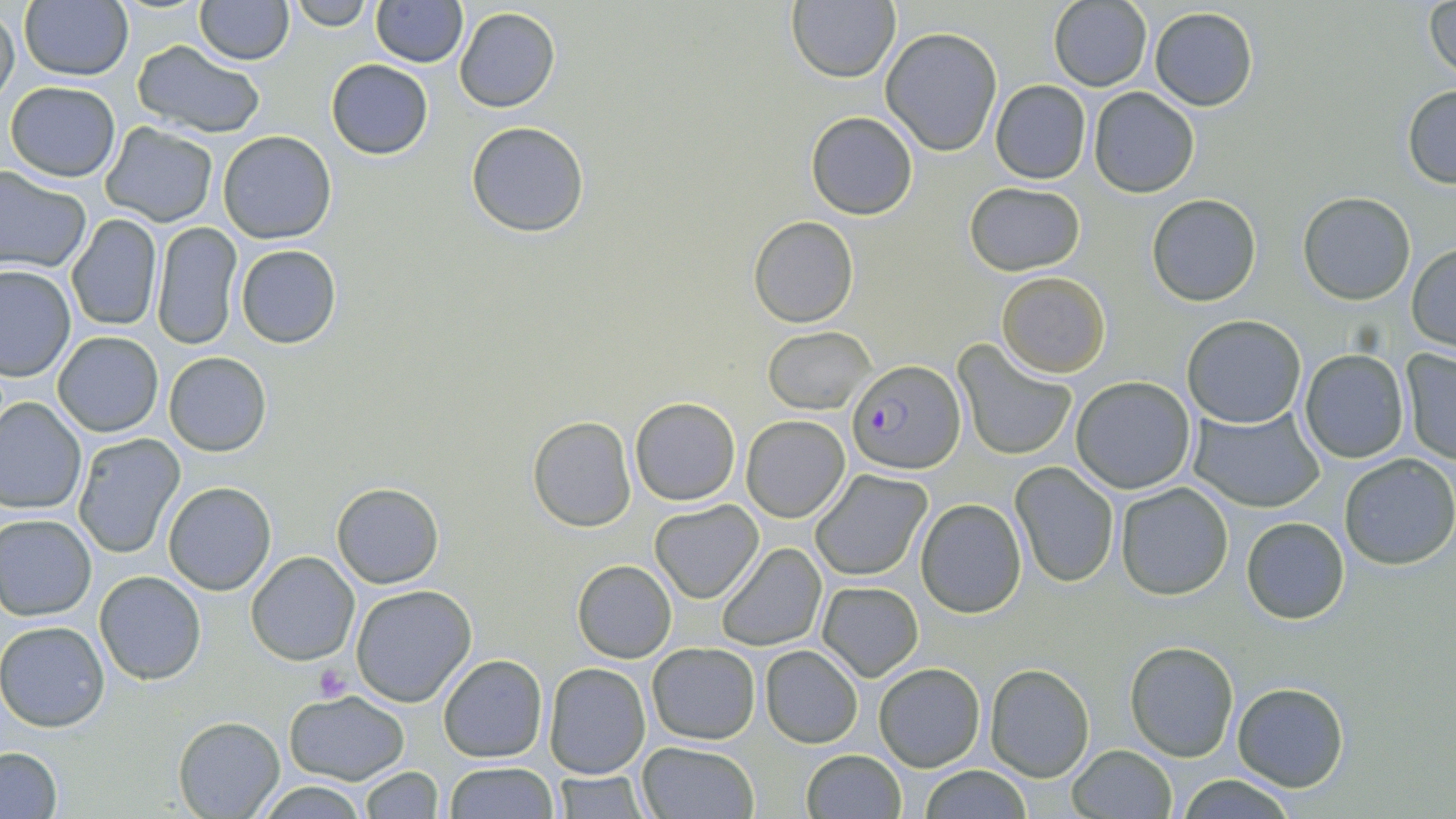
Summary:
  - Coordinate format: approximate bounding boxes as named x1/y1/x2/y2 corners in pixels
  - Platelet locations: (x1=312, y1=664, x2=351, y2=704)
  - Uninfected red blood cell locations: (x1=194, y1=0, x2=294, y2=65), (x1=291, y1=0, x2=375, y2=31), (x1=370, y1=0, x2=466, y2=67), (x1=1426, y1=0, x2=1456, y2=84), (x1=19, y1=1, x2=134, y2=82), (x1=359, y1=1, x2=457, y2=135), (x1=787, y1=1, x2=899, y2=82), (x1=1047, y1=1, x2=1153, y2=91), (x1=0, y1=7, x2=20, y2=109), (x1=454, y1=7, x2=560, y2=113), (x1=1149, y1=8, x2=1258, y2=111), (x1=881, y1=28, x2=1001, y2=157), (x1=133, y1=39, x2=263, y2=137), (x1=326, y1=59, x2=434, y2=159), (x1=5, y1=80, x2=121, y2=181), (x1=991, y1=81, x2=1091, y2=184), (x1=1403, y1=86, x2=1456, y2=188), (x1=1088, y1=88, x2=1198, y2=198), (x1=806, y1=111, x2=918, y2=221), (x1=466, y1=122, x2=591, y2=237), (x1=102, y1=123, x2=217, y2=228), (x1=218, y1=131, x2=337, y2=244), (x1=0, y1=167, x2=92, y2=274), (x1=964, y1=181, x2=1086, y2=275), (x1=1297, y1=192, x2=1417, y2=305), (x1=1147, y1=193, x2=1261, y2=306), (x1=64, y1=215, x2=163, y2=332), (x1=749, y1=216, x2=859, y2=329), (x1=151, y1=222, x2=242, y2=350), (x1=234, y1=244, x2=341, y2=349), (x1=1407, y1=245, x2=1456, y2=350), (x1=0, y1=265, x2=75, y2=381), (x1=994, y1=270, x2=1110, y2=378), (x1=1181, y1=314, x2=1307, y2=428), (x1=764, y1=327, x2=874, y2=413), (x1=52, y1=331, x2=164, y2=438), (x1=952, y1=339, x2=1077, y2=462), (x1=1400, y1=349, x2=1456, y2=463), (x1=1298, y1=350, x2=1409, y2=463), (x1=163, y1=352, x2=272, y2=457), (x1=1070, y1=375, x2=1196, y2=494), (x1=629, y1=395, x2=742, y2=506), (x1=0, y1=397, x2=87, y2=514), (x1=1188, y1=406, x2=1325, y2=513), (x1=741, y1=415, x2=850, y2=522), (x1=527, y1=417, x2=637, y2=532), (x1=74, y1=434, x2=185, y2=557), (x1=1339, y1=453, x2=1455, y2=569), (x1=1011, y1=462, x2=1119, y2=587), (x1=810, y1=469, x2=932, y2=581), (x1=163, y1=482, x2=276, y2=595), (x1=331, y1=482, x2=443, y2=587), (x1=1114, y1=483, x2=1234, y2=600), (x1=916, y1=499, x2=1027, y2=617), (x1=650, y1=501, x2=764, y2=603), (x1=0, y1=513, x2=98, y2=620), (x1=1241, y1=516, x2=1351, y2=624), (x1=716, y1=542, x2=826, y2=651), (x1=246, y1=551, x2=359, y2=663), (x1=573, y1=560, x2=676, y2=663), (x1=95, y1=571, x2=206, y2=685), (x1=817, y1=581, x2=924, y2=681), (x1=350, y1=584, x2=477, y2=706), (x1=0, y1=620, x2=110, y2=732), (x1=1125, y1=640, x2=1239, y2=760), (x1=646, y1=641, x2=761, y2=744), (x1=760, y1=646, x2=863, y2=748), (x1=438, y1=653, x2=548, y2=763), (x1=544, y1=663, x2=650, y2=779), (x1=874, y1=663, x2=986, y2=771), (x1=985, y1=663, x2=1094, y2=781), (x1=1231, y1=682, x2=1349, y2=791), (x1=283, y1=691, x2=410, y2=784), (x1=173, y1=715, x2=284, y2=817), (x1=635, y1=740, x2=760, y2=818), (x1=1067, y1=744, x2=1177, y2=818), (x1=0, y1=748, x2=61, y2=818), (x1=799, y1=749, x2=906, y2=819), (x1=443, y1=762, x2=560, y2=818), (x1=358, y1=766, x2=443, y2=819), (x1=918, y1=766, x2=1033, y2=818), (x1=551, y1=770, x2=649, y2=818), (x1=1171, y1=775, x2=1303, y2=817), (x1=255, y1=781, x2=370, y2=817)
  - Plasmodium falciparum-infected red blood cell locations: (x1=848, y1=361, x2=966, y2=476)
  - Slide-level diagnosis: Plasmodium falciparum
  - Stain: May-Grünwald-Giemsa
  - Preparation: thin blood film
  - Image size: 1456×819 pixels
  - Field of view: single
  - Modality: optical microscopy
  - Magnification: 1000x